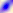 Photomicrograph. Toxoplasma gondii is seen. Captured at 400x magnification.